Point out each leukocyte.
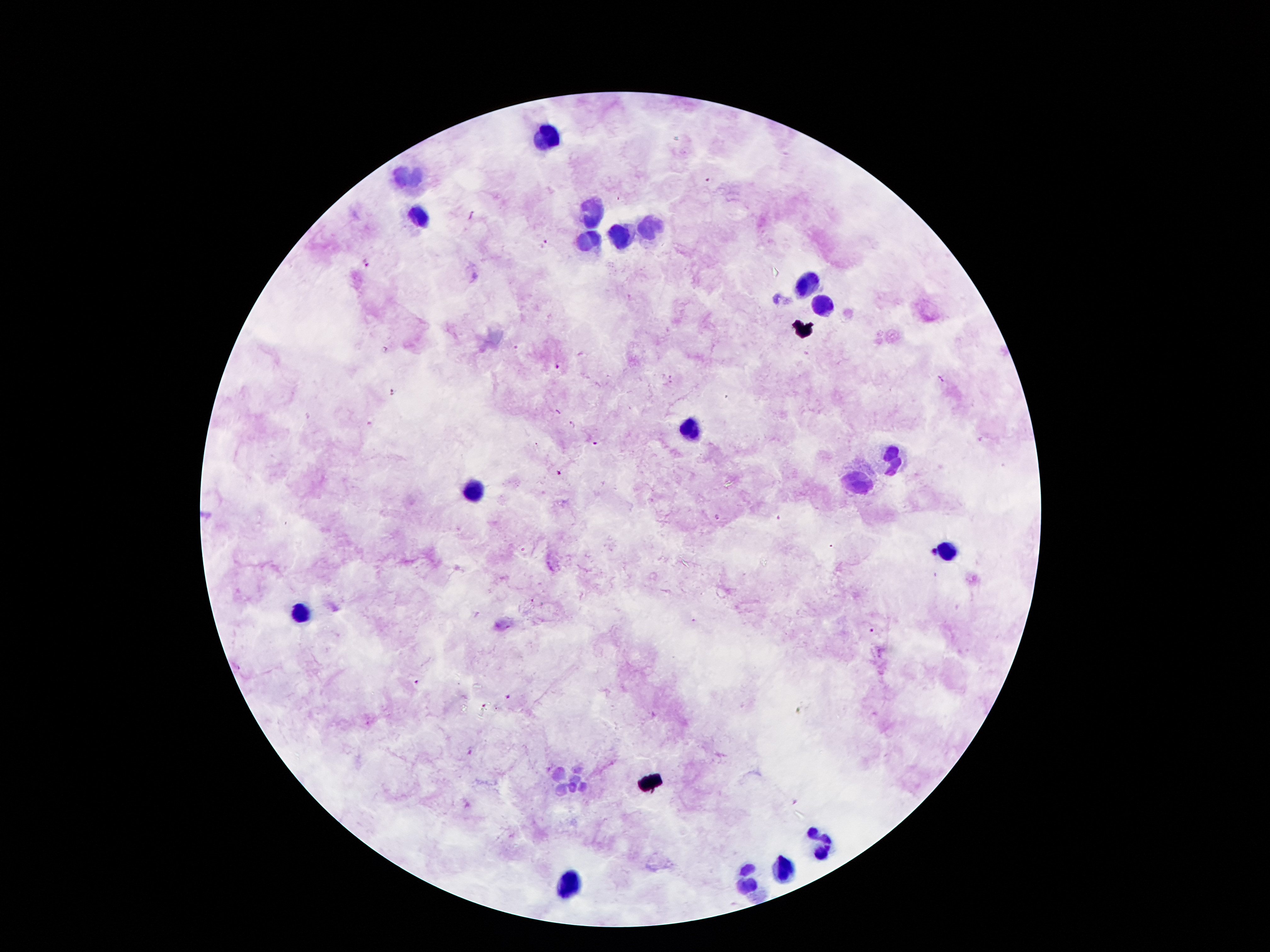

Approximate centers as [x, y] in pixels.
Leukocytes: [547, 139], [411, 176], [588, 214], [418, 217], [652, 226], [624, 235], [588, 241], [808, 285], [824, 305], [688, 430], [892, 458], [860, 483], [475, 489], [945, 551], [300, 612], [570, 782], [822, 846], [783, 871], [749, 878], [570, 884].

Malaria parasite locations: [709, 181], [472, 214], [545, 244], [367, 263], [630, 297], [386, 350], [516, 350], [559, 367], [668, 377], [939, 377], [669, 383], [392, 392], [572, 425], [597, 443], [560, 472], [718, 517], [778, 518], [934, 551], [695, 620], [871, 631], [414, 682], [510, 699], [796, 802]. Giemsa stain. Smartphone photograph taken through the microscope eyepiece. Patient malaria status: positive for Plasmodium falciparum. One field from this slide. Image is 1270×952 pixels. Thick blood smear. 100x magnification.